Outline each Plasmodium falciparum-infected red blood cell.
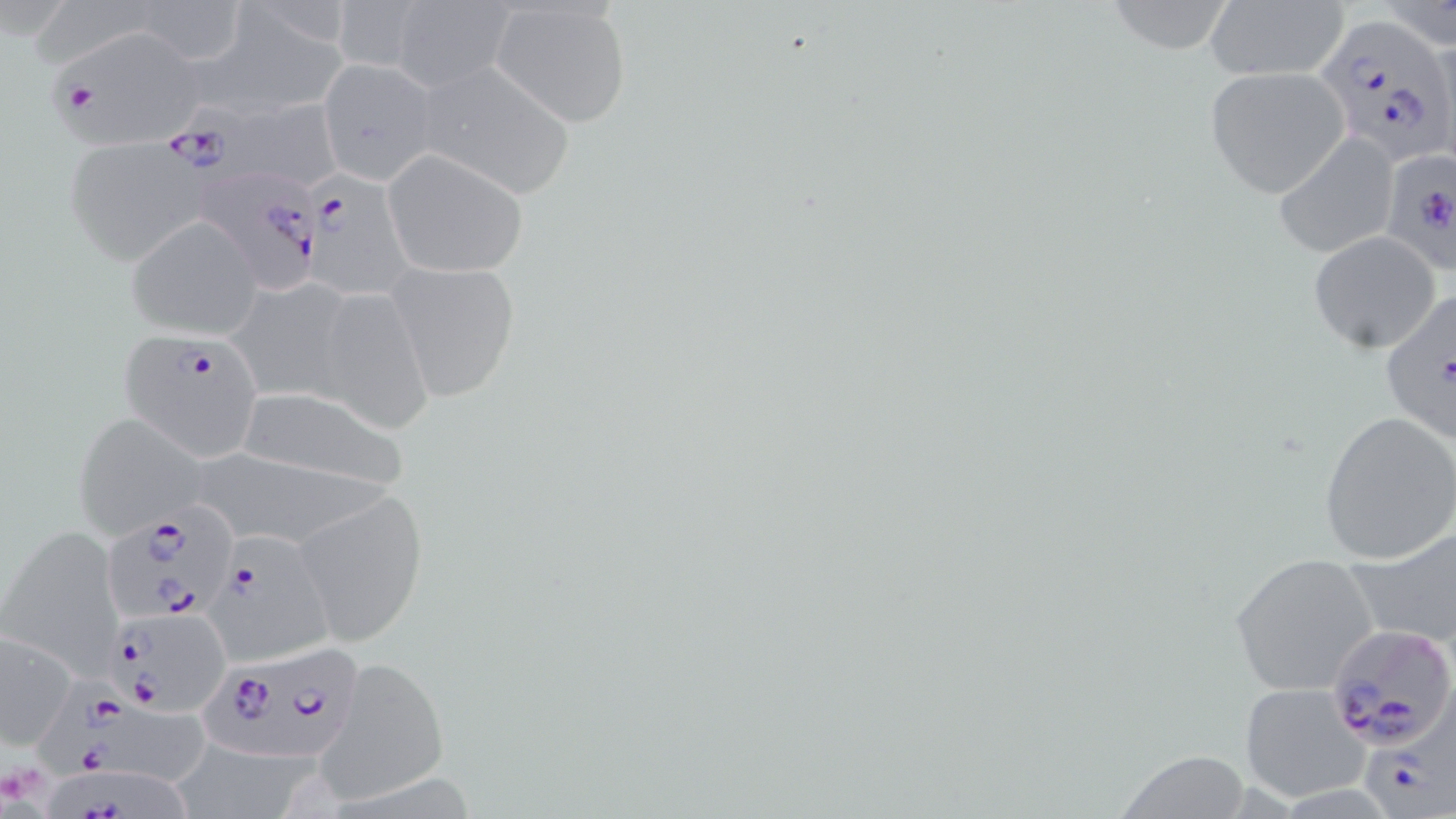
Approximate bounding boxes as [x1, y1, x2, y2] in pixels.
Plasmodium falciparum-infected red blood cells: [1311, 11, 1453, 165], [41, 23, 212, 152], [63, 105, 241, 265], [1381, 144, 1456, 275], [299, 163, 424, 302], [199, 165, 328, 289], [1379, 288, 1454, 441], [119, 327, 266, 458], [98, 507, 235, 650], [210, 533, 332, 667], [108, 607, 233, 713], [1326, 622, 1456, 750], [196, 639, 366, 762], [29, 678, 220, 788], [1365, 690, 1456, 815], [36, 759, 210, 819].

slide-level diagnosis = Plasmodium falciparum
field of view = one of a larger specimen
uninfected red blood cell locations = approximate bounding boxes as [x1, y1, x2, y2] in pixels: [129, 0, 249, 67], [328, 0, 423, 76], [1203, 0, 1351, 84], [390, 1, 516, 91], [1101, 1, 1238, 55], [491, 2, 634, 128], [1377, 4, 1456, 50], [203, 7, 352, 117], [321, 55, 439, 185], [412, 62, 577, 198], [1204, 67, 1351, 198], [225, 96, 348, 194], [1272, 132, 1401, 260], [383, 151, 528, 278], [126, 217, 260, 339], [1309, 232, 1440, 354], [385, 261, 521, 403], [228, 277, 359, 404], [314, 287, 434, 435], [229, 388, 414, 494], [1318, 411, 1456, 566], [71, 412, 209, 539], [295, 486, 428, 647], [1345, 523, 1456, 651], [2, 525, 125, 676], [1228, 552, 1383, 697], [1, 630, 78, 750], [318, 658, 451, 805], [1239, 684, 1367, 805], [182, 736, 319, 819], [1108, 753, 1254, 817]
magnification = 1000x
stain = May-Grünwald-Giemsa
platelet locations = approximate bounding boxes as [x1, y1, x2, y2] in pixels: [0, 763, 46, 807]
image size = 1456×819 pixels
modality = light microscopy
preparation = thin blood smear